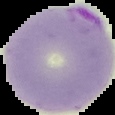
image_type: segmented cell region with the area outside set to black
preparation: thin blood film
image_size: 115×115 pixels
malaria_status: parasitized